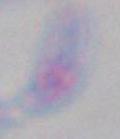

identification: Toxoplasma gondii
modality: micrograph
magnification: 1000x